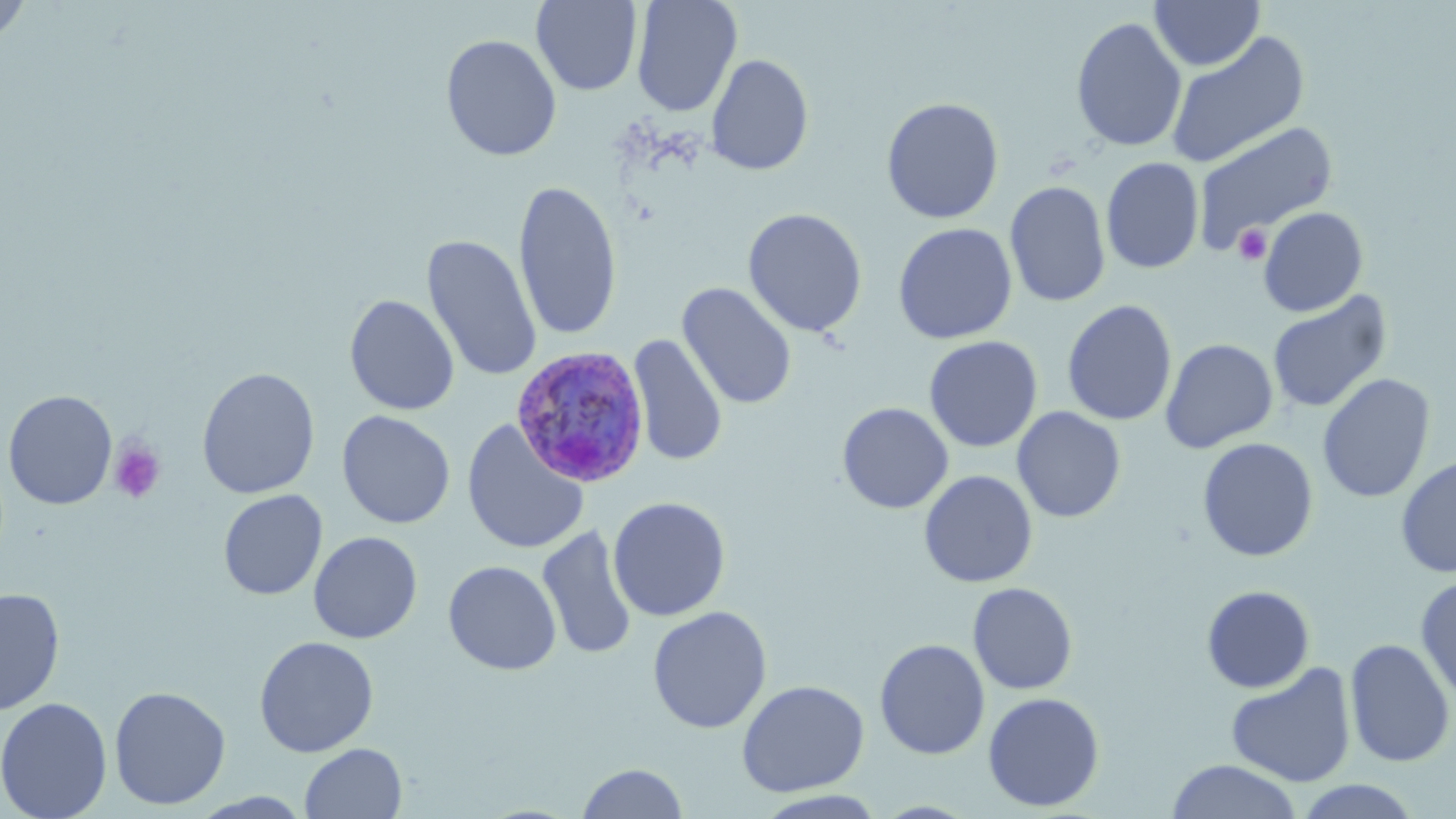
Plasmodium ovale-infected red blood cell locations = approximate bounding boxes as (x1, y1, x2, y2) in pixels: (510, 345, 650, 488)
slide-level diagnosis = Plasmodium ovale
platelet locations = approximate bounding boxes as (x1, y1, x2, y2) in pixels: (1234, 224, 1272, 264), (108, 440, 166, 504)
image size = 1456×819 pixels
preparation = thin blood smear
stain = May-Grünwald-Giemsa
modality = optical microscopy
magnification = 1000x
uninfected red blood cell locations = approximate bounding boxes as (x1, y1, x2, y2) in pixels: (0, 0, 34, 47), (631, 0, 742, 117), (1149, 0, 1265, 71), (530, 1, 643, 96), (1070, 15, 1187, 153), (1164, 31, 1310, 168), (441, 34, 562, 161), (705, 54, 814, 176), (881, 97, 1004, 224), (1193, 122, 1338, 252), (1101, 156, 1204, 274), (513, 180, 623, 341), (1004, 180, 1111, 308), (1258, 206, 1368, 317), (742, 208, 868, 338), (893, 223, 1017, 344), (422, 234, 542, 382), (677, 283, 797, 410), (1267, 291, 1392, 414), (345, 294, 459, 416), (1061, 299, 1178, 427), (628, 333, 728, 468), (924, 336, 1043, 452), (1160, 338, 1278, 453), (196, 367, 320, 499), (1317, 373, 1435, 503), (2, 389, 118, 510), (837, 402, 954, 514), (1012, 406, 1126, 522), (337, 410, 455, 529), (461, 419, 589, 555), (1197, 438, 1319, 561), (1396, 455, 1455, 579), (919, 470, 1038, 588), (218, 490, 327, 600), (608, 496, 731, 622), (537, 526, 638, 661), (308, 531, 423, 644), (443, 561, 561, 674), (1415, 575, 1456, 706), (967, 582, 1078, 695), (1201, 585, 1315, 693), (0, 587, 65, 715), (647, 606, 772, 734), (254, 635, 379, 757), (1345, 637, 1455, 768), (874, 638, 990, 760), (1225, 662, 1357, 788), (736, 679, 869, 797), (108, 685, 231, 810), (983, 692, 1104, 811), (0, 697, 113, 819), (299, 743, 407, 819), (1165, 759, 1303, 819), (577, 762, 688, 819), (1294, 779, 1423, 818), (754, 790, 888, 818)
field of view = single